Identify the preparation type.
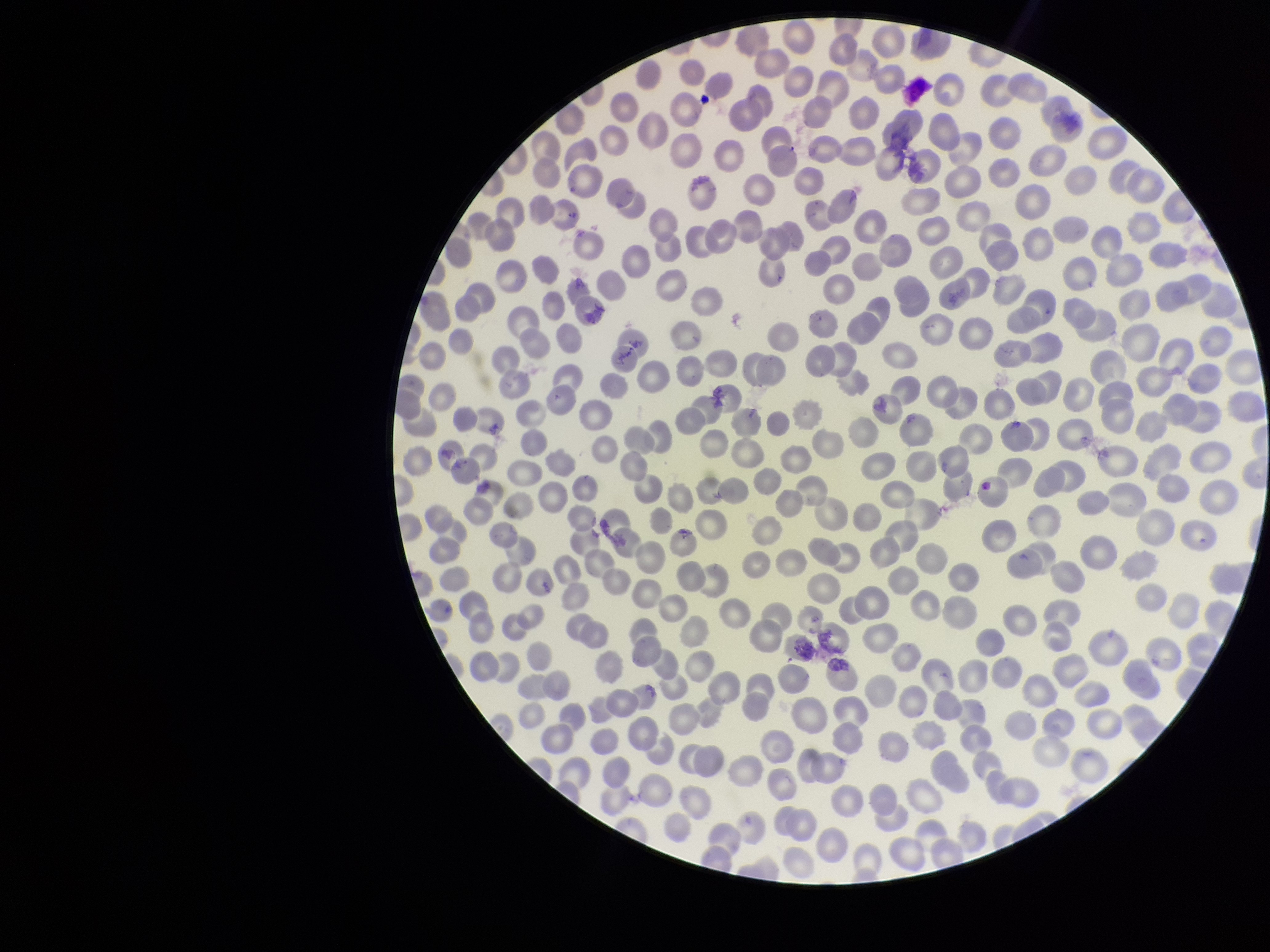
It is a thin blood smear.

Summary:
  - Stain: Giemsa
  - Field of view: one from this slide
  - Red blood cell count: 322
  - Patient malaria status: infected
  - Image size: 1270×952 pixels
  - Parasitized red blood cell count: 0
  - Species reported for this patient: Plasmodium vivax
  - Capture: smartphone photograph through the microscope eyepiece
  - Parasitized red blood cells: none seen